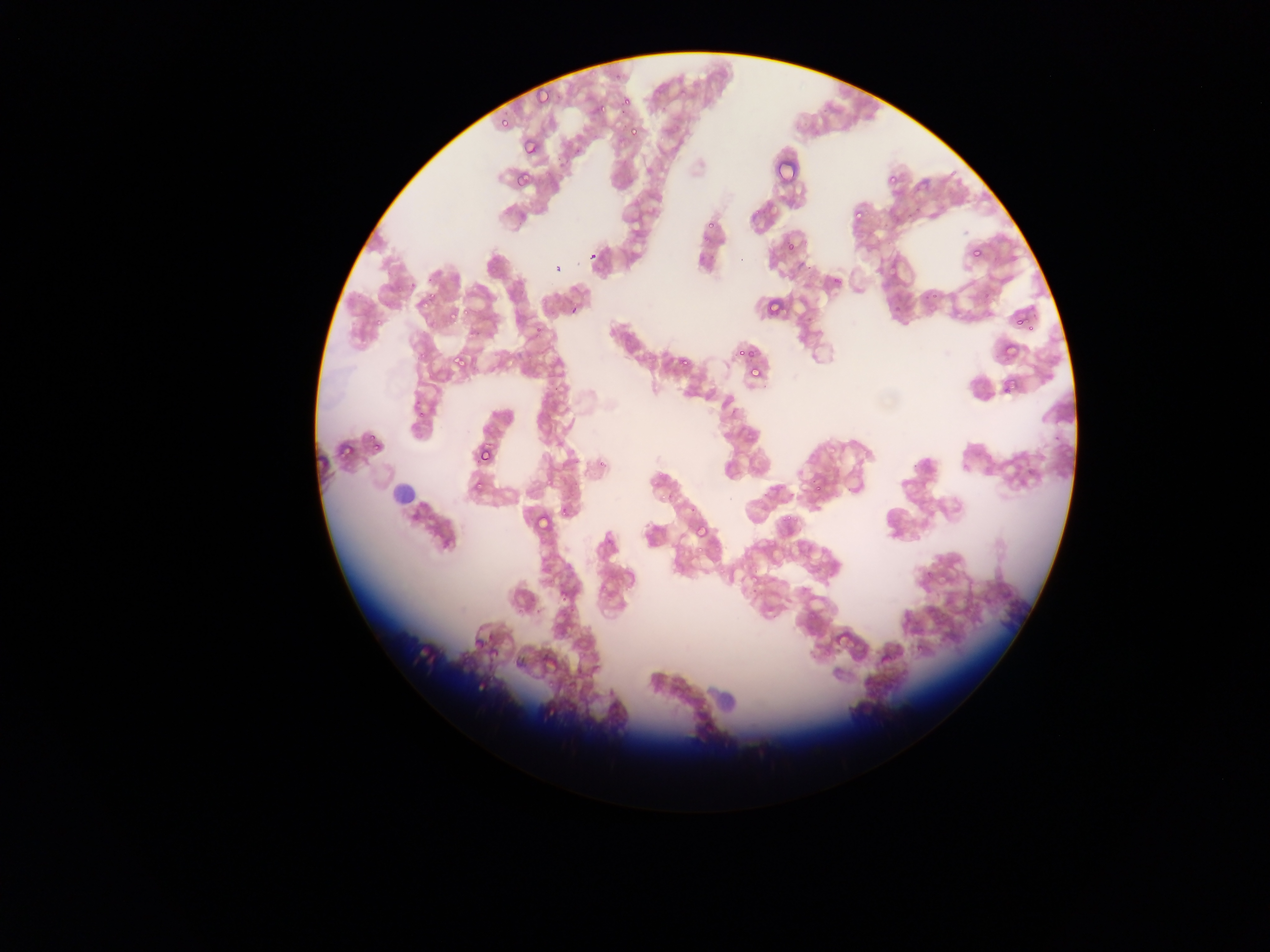
capture = mobile-phone photograph through a microscope
field of view = single
country = Ghana
Plasmodium parasite locations = approximate bounding boxes as [left, top, right, bottom] in pixels: [532, 82, 545, 105], [616, 94, 628, 105], [594, 105, 610, 120], [496, 117, 512, 131], [625, 118, 642, 135], [518, 139, 535, 156], [882, 167, 904, 185], [507, 172, 530, 187], [848, 206, 867, 224], [697, 219, 720, 232], [782, 239, 805, 256], [965, 242, 982, 256], [415, 293, 435, 309], [766, 298, 784, 318], [1014, 308, 1024, 325], [443, 310, 465, 327], [1004, 341, 1022, 356], [731, 346, 754, 356], [444, 350, 476, 375], [677, 355, 694, 370], [744, 361, 764, 379], [1001, 382, 1015, 396], [365, 435, 377, 451], [337, 443, 350, 459], [478, 446, 494, 464], [467, 473, 490, 491], [533, 513, 553, 528], [693, 521, 714, 540], [485, 643, 509, 661]
image size = 1270×952 pixels
preparation = thin blood film